State which parasite is depicted.
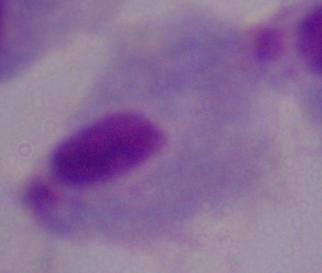
This is a trichomonad.

Photomicrograph. 1000x magnification.